Describe the morphology of the red blood cells.
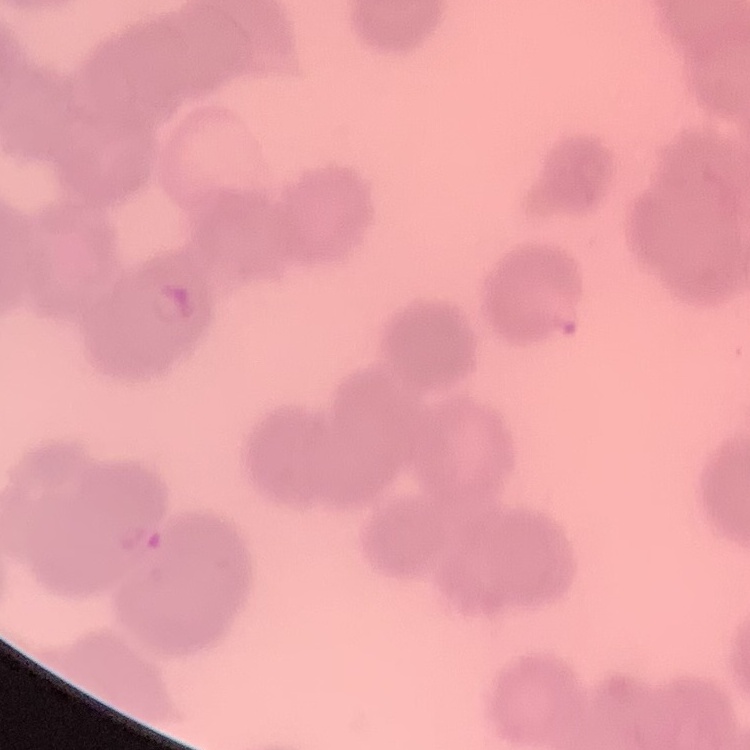
They show rouleaux formation.

Summary:
  - Stain: Field's or Giemsa
  - Image type: square crop of a larger photomicrograph
  - Preparation: thin peripheral smear